Locate every blood parasite and identify its species.
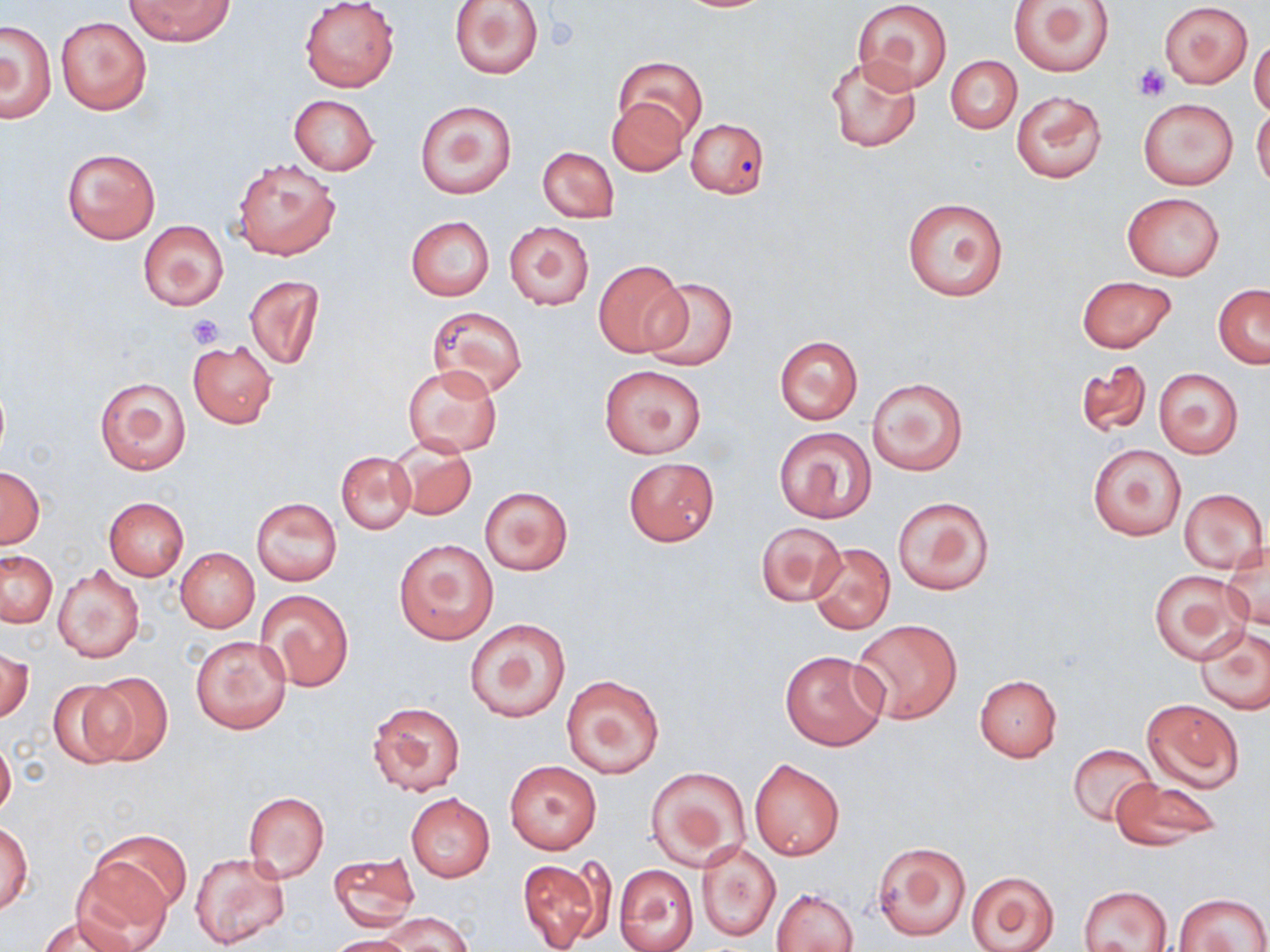
No blood parasites observed.

Approximate bounding boxes as (x1,y1)-(x2,y2) corner pairs in pixels. Uninfected red blood cell locations: (126,0)-(233,46), (299,0)-(399,91), (449,0)-(545,79), (853,0)-(951,92), (1009,0)-(1116,77), (1160,2)-(1252,87), (54,16)-(152,116), (1,20)-(56,123), (1250,37)-(1270,117), (945,53)-(1022,134), (824,54)-(922,154), (614,55)-(707,144), (1012,90)-(1105,183), (287,94)-(380,174), (606,98)-(689,177), (1139,98)-(1238,190), (415,101)-(517,199), (1252,106)-(1270,189), (685,116)-(770,197), (63,147)-(160,244), (538,147)-(618,223), (232,159)-(342,261), (1123,192)-(1224,280), (902,197)-(1008,302), (405,217)-(494,300), (138,220)-(228,310), (504,220)-(595,311), (591,258)-(691,357), (246,275)-(324,371), (1077,276)-(1176,353), (640,278)-(739,371), (1212,284)-(1269,367), (426,306)-(528,399), (774,335)-(863,426), (188,340)-(277,428), (1075,359)-(1153,440), (403,364)-(503,456), (598,364)-(707,458), (1153,367)-(1245,460), (95,375)-(191,475), (866,377)-(968,475), (774,427)-(877,523), (389,439)-(477,520), (1086,444)-(1186,541), (336,452)-(416,534), (622,457)-(718,547), (0,467)-(45,549), (480,485)-(574,576), (1180,487)-(1268,573), (891,495)-(995,596), (104,497)-(189,580), (251,497)-(342,585), (755,521)-(846,605), (394,538)-(498,644), (807,542)-(896,636), (1223,546)-(1269,630), (176,549)-(259,632), (1,551)-(58,628), (53,563)-(145,663), (1149,570)-(1249,663), (257,589)-(353,691), (464,616)-(571,723), (852,620)-(962,724), (1195,626)-(1270,715), (191,635)-(292,734), (0,647)-(33,725), (779,649)-(888,750), (83,671)-(172,767), (561,675)-(664,778), (974,675)-(1061,761), (46,680)-(136,770), (1143,698)-(1244,791), (367,700)-(465,797), (0,736)-(16,819), (1068,744)-(1159,828), (505,759)-(602,854), (749,759)-(844,860), (645,766)-(749,869), (1110,778)-(1220,851), (243,791)-(329,882), (405,793)-(494,882), (1,822)-(33,913), (96,829)-(189,917), (873,841)-(971,941), (696,843)-(780,941), (328,852)-(420,930), (190,853)-(289,950), (517,857)-(608,952), (72,863)-(172,950), (613,864)-(697,952), (966,869)-(1059,951), (1078,885)-(1172,951), (772,888)-(858,952), (1176,892)-(1268,952), (383,912)-(473,952), (38,914)-(135,952), (323,935)-(421,952). Platelet locations: (1133,64)-(1172,100), (185,313)-(227,348). Slide-level diagnosis: no evidence of blood parasites. Thin blood smear. One field of a larger specimen. Captured at 1000x magnification. Image is 1270×952 pixels. Light microscopy. May-Grünwald-Giemsa-stained preparation.